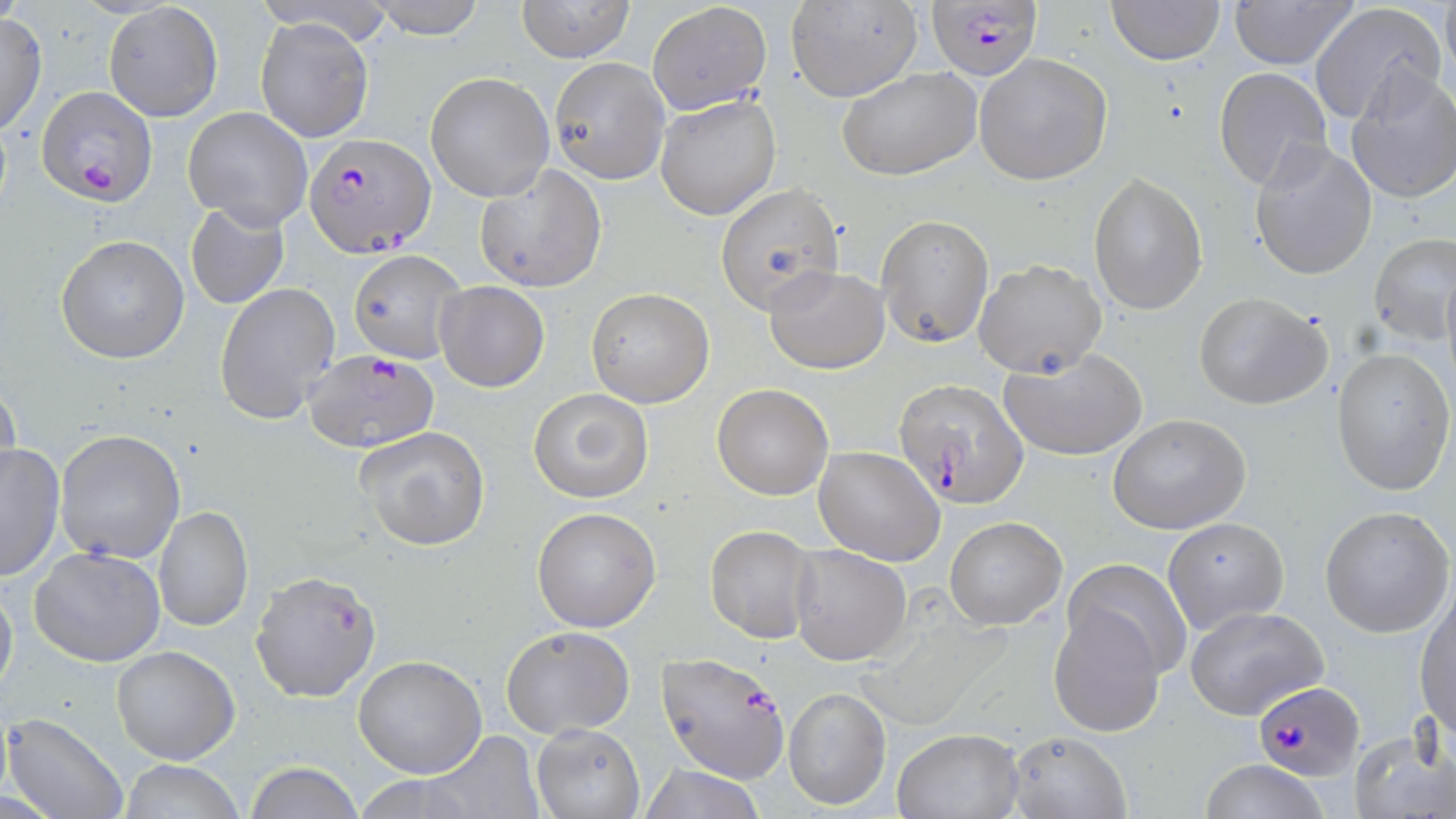

slide-level diagnosis = Plasmodium falciparum
uninfected red blood cell locations = approximate bounding boxes as (x1, y1, x2, y2) in pixels: (362, 0, 490, 39), (516, 0, 636, 65), (788, 0, 922, 103), (1104, 0, 1227, 65), (1227, 0, 1363, 69), (1440, 0, 1455, 80), (648, 1, 770, 113), (103, 2, 224, 122), (1309, 3, 1447, 124), (0, 13, 47, 135), (256, 18, 374, 143), (974, 54, 1112, 185), (550, 58, 669, 181), (836, 64, 985, 182), (1213, 67, 1333, 192), (1344, 70, 1456, 204), (425, 72, 555, 202), (656, 92, 782, 221), (183, 106, 313, 231), (1249, 138, 1378, 281), (475, 163, 607, 294), (1089, 175, 1207, 313), (716, 183, 844, 313), (185, 201, 291, 311), (877, 214, 995, 347), (55, 234, 189, 364), (1368, 234, 1454, 345), (348, 248, 466, 365), (973, 256, 1107, 378), (763, 265, 891, 374), (434, 281, 549, 391), (215, 283, 342, 423), (585, 288, 714, 408), (1194, 291, 1332, 411), (999, 348, 1150, 461), (1332, 348, 1454, 495), (0, 379, 21, 490), (711, 383, 834, 500), (528, 387, 654, 503), (1107, 415, 1250, 534), (354, 426, 491, 551), (54, 429, 185, 563), (0, 441, 65, 582), (813, 445, 945, 565), (154, 506, 253, 632), (532, 506, 660, 631), (1321, 507, 1455, 638), (944, 516, 1066, 630), (1162, 517, 1288, 634), (704, 525, 818, 645), (788, 544, 911, 665), (30, 545, 166, 667), (1064, 558, 1192, 679), (0, 580, 18, 706), (1415, 587, 1456, 740), (1046, 603, 1166, 737), (1184, 606, 1329, 719), (500, 626, 635, 738), (111, 646, 240, 766), (353, 654, 487, 777), (782, 684, 892, 810), (4, 712, 128, 819), (532, 724, 645, 818), (892, 728, 1023, 818), (1349, 728, 1454, 819), (422, 730, 542, 817), (1005, 730, 1131, 819), (1195, 759, 1332, 819), (118, 760, 246, 818), (245, 761, 364, 819), (635, 762, 769, 818), (354, 775, 486, 816)
magnification = 1000x
Plasmodium falciparum-infected red blood cell locations = approximate bounding boxes as (x1, y1, x2, y2) in pixels: (924, 1, 1046, 82), (36, 84, 155, 205), (303, 133, 434, 255), (302, 348, 439, 454), (894, 380, 1029, 508), (250, 570, 383, 703), (657, 650, 790, 781), (1252, 681, 1365, 780)
stain = May-Grünwald-Giemsa
modality = optical microscopy
preparation = thin blood film
image size = 1456×819 pixels
field of view = one of a larger specimen